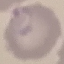

Malaria status: parasitized. Cell patch, automatically extracted from a larger field of view and resized to 64 × 64 pixels. Acquired by smartphone through the microscope eyepiece. Thin blood film. Giemsa stain.